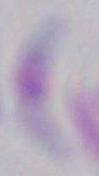

1000x magnification. Micrograph. Toxoplasma gondii is shown.